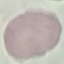
Result: negative for malaria parasites. Thin smear of blood. Automatically extracted cell patch, resized to 64 × 64 pixels. Acquired by smartphone through the microscope eyepiece. Giemsa-stained preparation.